Classify this cell by malaria status.
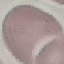
It is uninfected.

Summary:
  - Capture: smartphone camera at the microscope eyepiece
  - Stain: Giemsa
  - Image type: cell patch, automatically extracted from a larger field of view and resized to 64 × 64 pixels
  - Preparation: thin blood film